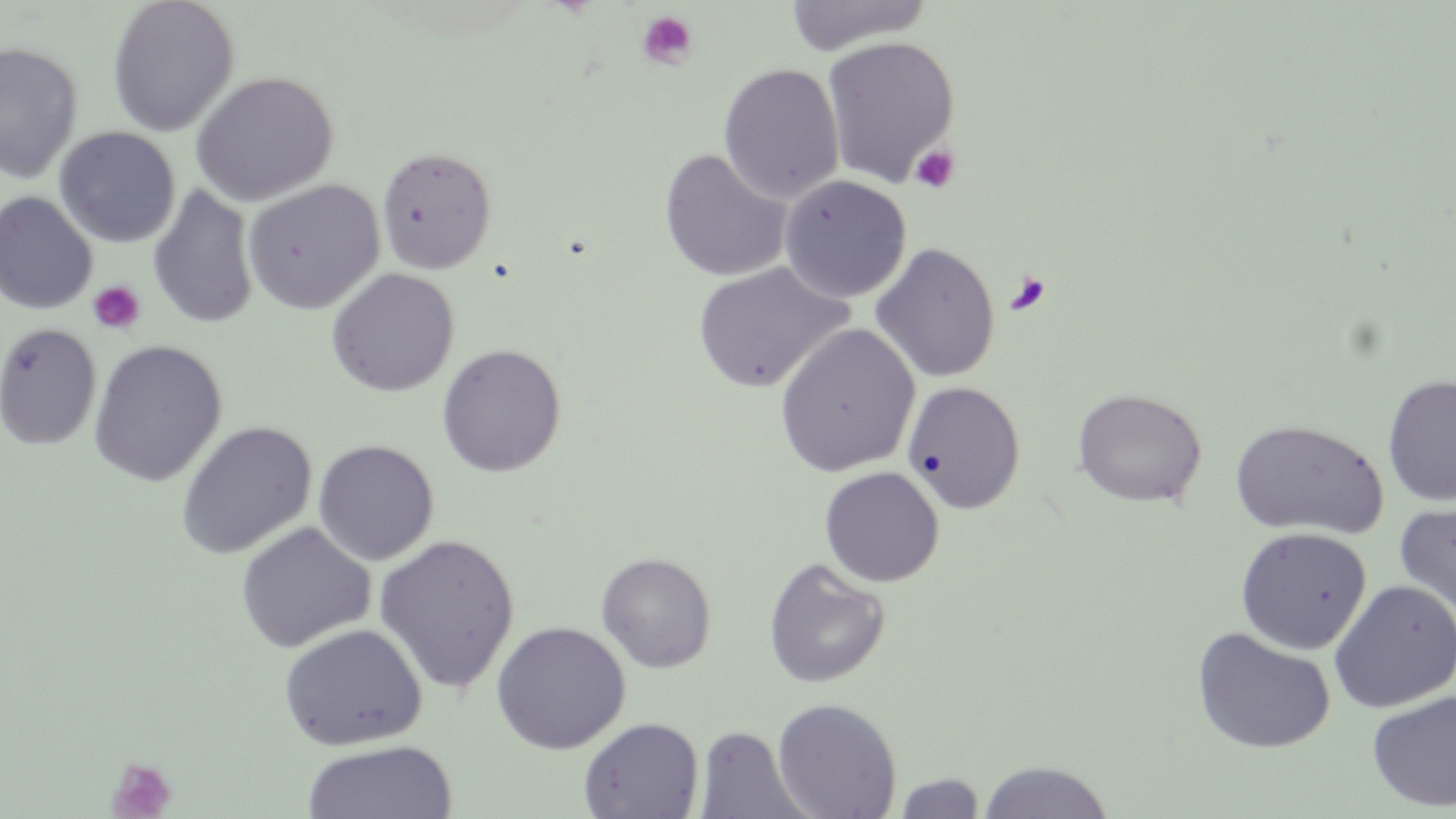

Approximate bounding boxes as (x1,y1)-(x2,y2) corner pairs in pixels. Platelet locations: (636,10)-(698,69), (910,145)-(961,193), (1004,272)-(1052,316), (87,280)-(146,335), (105,758)-(177,819). Uninfected red blood cell locations: (106,0)-(240,137), (783,0)-(934,56), (821,36)-(960,189), (0,42)-(82,184), (718,62)-(844,204), (190,71)-(339,206), (54,127)-(180,248), (376,146)-(497,275), (659,148)-(792,282), (778,175)-(912,303), (242,179)-(385,314), (147,185)-(259,329), (0,192)-(98,315), (870,242)-(1000,384), (692,261)-(852,393), (326,268)-(460,396), (0,323)-(102,450), (773,323)-(920,478), (88,339)-(227,487), (436,344)-(567,477), (1382,375)-(1456,507), (902,381)-(1025,513), (1072,388)-(1207,507), (1229,419)-(1387,539), (176,421)-(317,560), (313,439)-(439,566), (819,466)-(945,588), (1394,500)-(1456,624), (236,522)-(375,653), (1235,526)-(1372,655), (373,534)-(520,695), (596,551)-(717,673), (762,557)-(891,689), (1329,579)-(1456,713), (491,621)-(631,754), (276,623)-(428,750), (1192,627)-(1335,754), (1367,689)-(1456,812), (771,697)-(902,819), (579,716)-(703,819), (694,724)-(810,818), (301,739)-(457,819), (978,759)-(1114,818), (892,772)-(986,818). Slide-level diagnosis: negative for blood parasites. May-Grünwald-Giemsa-stained preparation. Thin blood smear. Image is 1456×819 pixels. 1000x magnification. One field of a larger specimen. Light microscopy.